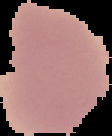

result = negative for malaria parasites
preparation = thin blood smear
image size = 112×136 pixels
image type = segmented cell region with the area outside set to black